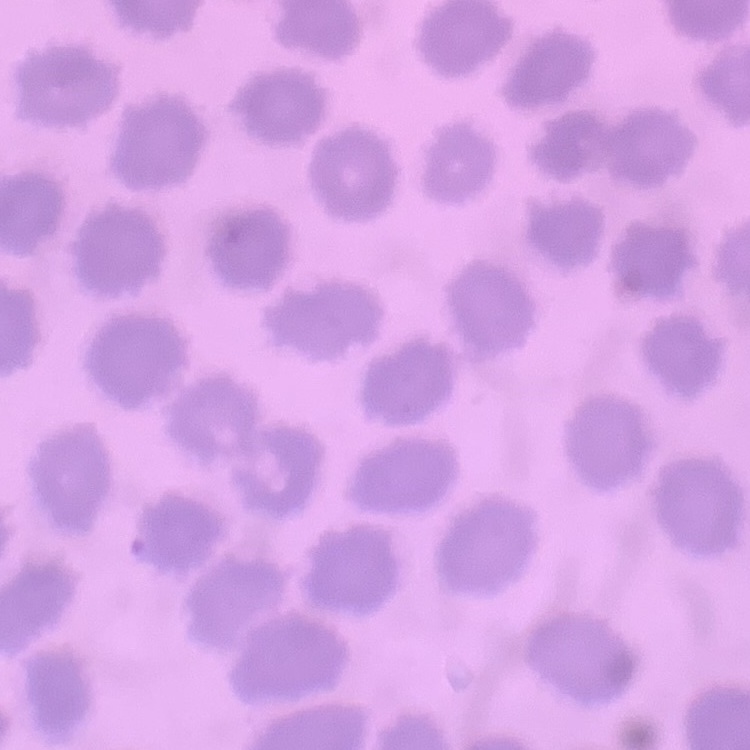

Summary:
  - Erythrocyte morphology: no rouleaux formation
  - Image type: one tile cut from a larger photomicrograph
  - Preparation: thin peripheral smear
  - Stain: Field's or Giemsa